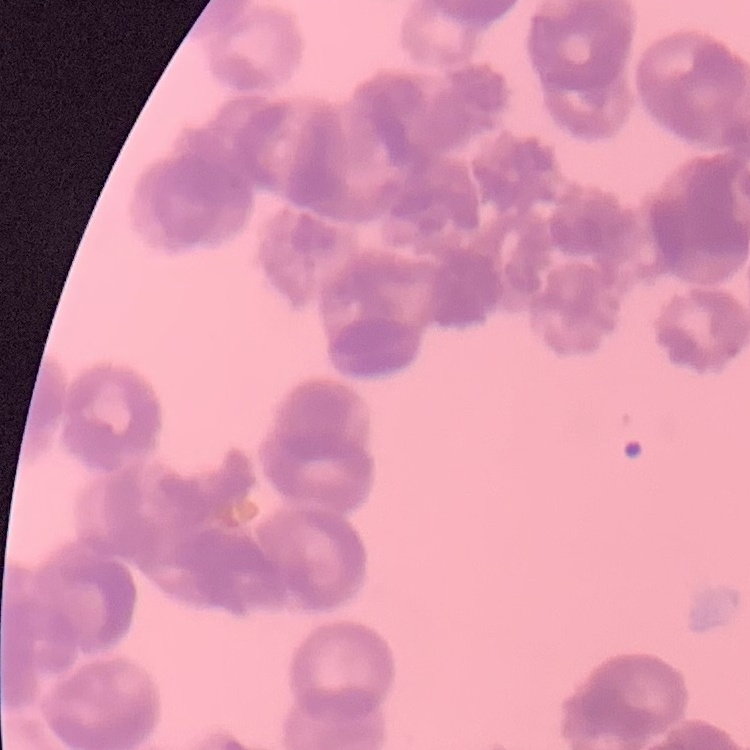

erythrocyte_morphology: rouleaux formation
preparation: thin blood film
image_type: one tile cut from a larger photomicrograph
stain: Field's or Giemsa